Locate platelets.
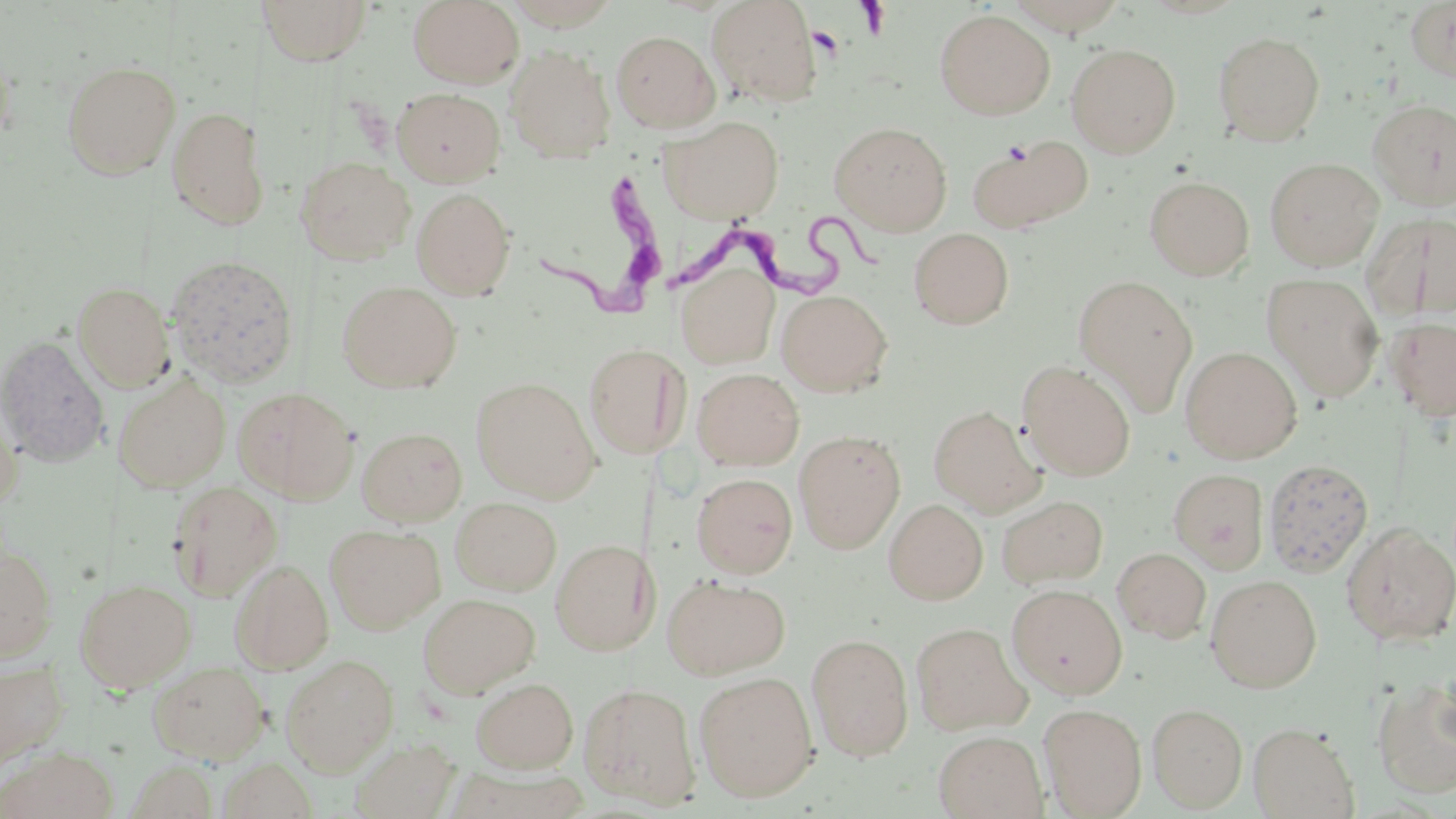
Approximate bounding boxes as (x1,y1)-(x2,y2) corner pairs in pixels.
Platelets: (807,26)-(845,59).

slide-level diagnosis = Trypanosoma brucei
image size = 1456×819 pixels
uninfected red blood cell locations = approximate bounding boxes as (x1,y1)-(x2,y2) corner pairs in pixels: (258,0)-(373,65), (408,0)-(525,88), (501,0)-(624,30), (706,0)-(821,106), (1003,0)-(1130,34), (1405,1)-(1456,83), (935,9)-(1055,119), (611,30)-(720,132), (1213,31)-(1326,145), (0,39)-(15,155), (1066,43)-(1181,157), (506,45)-(615,162), (61,60)-(180,179), (391,87)-(506,187), (1368,99)-(1456,210), (167,106)-(270,230), (662,115)-(784,224), (829,122)-(952,234), (967,135)-(1093,234), (296,156)-(415,265), (1265,157)-(1384,270), (1144,175)-(1254,280), (411,188)-(516,299), (1364,212)-(1456,320), (909,227)-(1014,329), (165,254)-(299,388), (675,262)-(780,369), (1262,273)-(1384,401), (1073,275)-(1199,415), (338,280)-(461,392), (72,281)-(175,392), (778,289)-(892,396), (1387,316)-(1456,421), (0,335)-(110,467), (584,343)-(689,458), (1181,346)-(1302,463), (1019,362)-(1136,480), (692,368)-(804,470), (114,375)-(231,492), (472,377)-(600,502), (234,386)-(358,502), (0,395)-(24,510), (928,405)-(1043,515), (356,426)-(467,526), (794,430)-(905,553), (1263,458)-(1373,576), (1169,469)-(1269,573), (692,472)-(798,577), (167,481)-(283,600), (997,494)-(1108,589), (451,497)-(562,595), (884,499)-(988,604), (1342,523)-(1456,647), (325,524)-(445,634), (550,539)-(658,654), (0,546)-(57,663), (1113,548)-(1211,643), (230,559)-(334,674), (663,574)-(791,679), (1205,575)-(1322,692), (75,578)-(196,692), (1008,584)-(1127,699), (419,593)-(540,698), (910,622)-(1031,736), (807,633)-(914,760), (280,654)-(399,775), (0,658)-(69,770), (148,661)-(269,763), (694,671)-(818,801), (471,677)-(578,772), (1373,677)-(1456,797), (579,682)-(701,808), (1039,703)-(1147,818), (1147,703)-(1248,812), (1248,721)-(1359,818), (933,731)-(1046,818), (352,738)-(459,818), (1,747)-(119,819), (217,758)-(317,818), (128,760)-(220,818)
magnification = 1000x
field of view = one of a larger specimen
modality = optical microscopy
stain = May-Grünwald-Giemsa
preparation = thin blood smear
Trypanosoma brucei locations = approximate bounding boxes as (x1,y1)-(x2,y2) corner pairs in pixels: (518,158)-(669,318), (672,211)-(897,309)